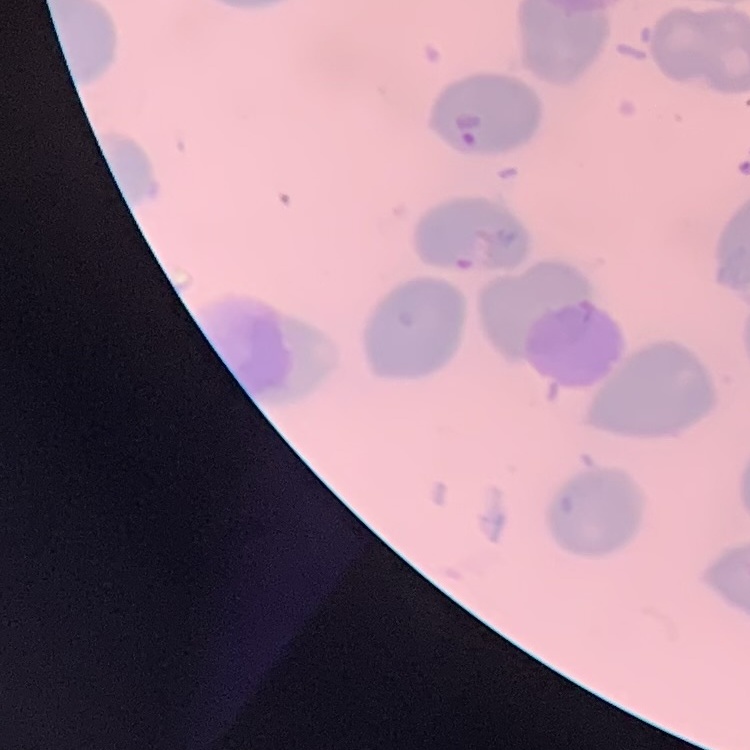

{
  "red_blood_cell_morphology": "no rouleaux formation",
  "image_type": "one tile cut from a larger photomicrograph",
  "stain": "Field's or Giemsa",
  "preparation": "thin peripheral smear"
}